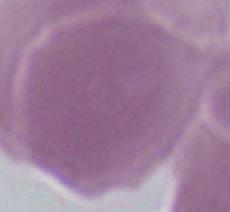

Photomicrograph. A red blood cell is shown. 1000x magnification.